Describe the morphology of the red blood cells.
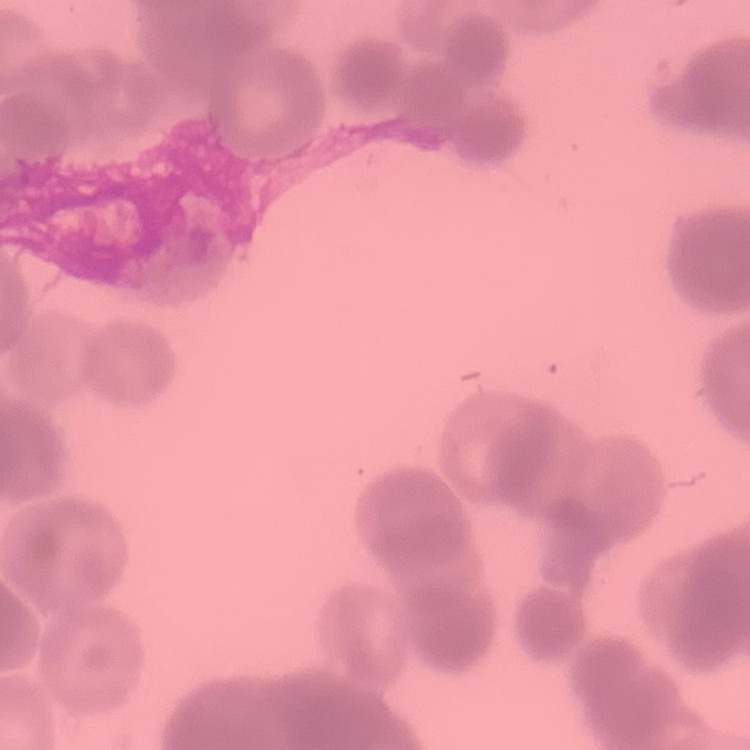

Rouleaux formation.

image type = square crop of a larger photomicrograph
preparation = thin blood film
stain = Field's or Giemsa